Classify this cell by malaria status.
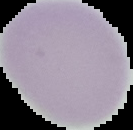

Uninfected.

Summary:
  - Image size: 133×130 pixels
  - Image type: segmented cell region on a black background
  - Preparation: thin blood film